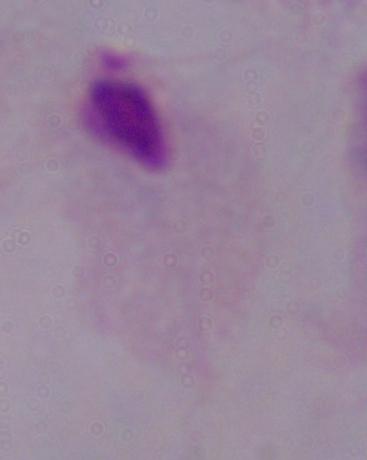

{
  "identification": "trichomonad",
  "modality": "micrograph",
  "magnification": "1000x"
}